Describe the morphology of the erythrocytes.
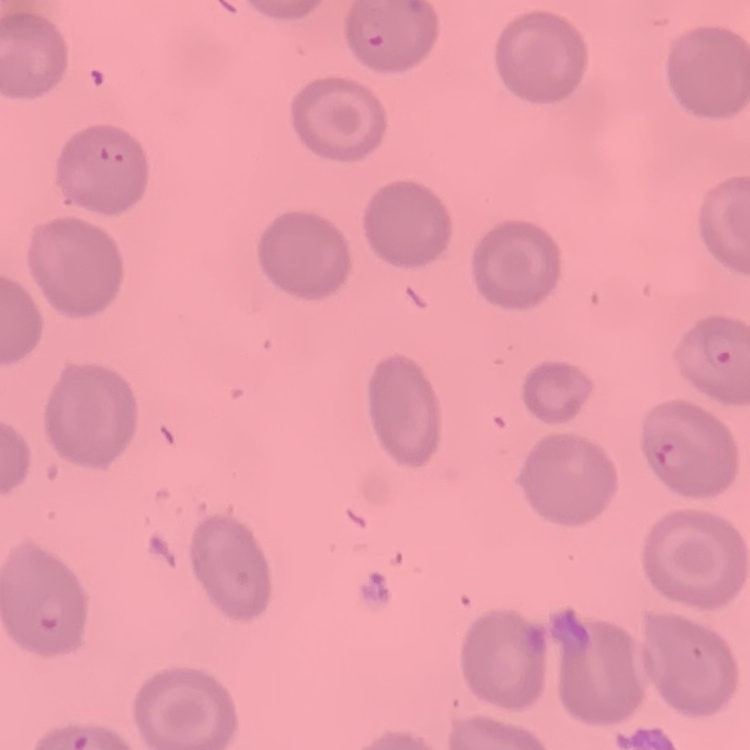

No rouleaux formation.

Summary:
  - Preparation: thin blood film
  - Image type: square crop of a larger photomicrograph
  - Stain: Field's or Giemsa